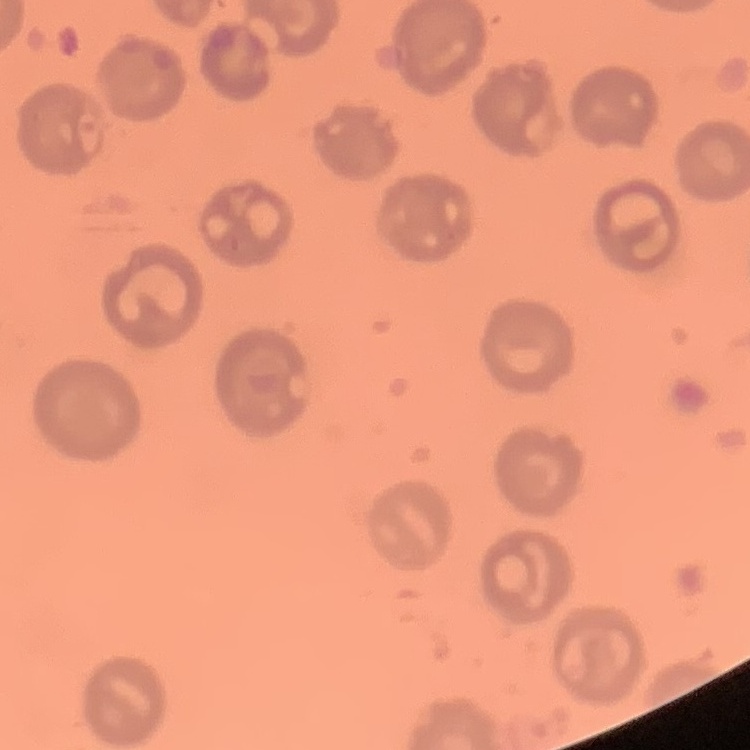

The red blood cells show no rouleaux formation. One tile cut from a larger photomicrograph. Stained with either Field's or Giemsa. Thin blood smear.